Classify this cell by malaria status.
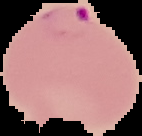

Parasitized.

image type = cell region segmented out of the field of view; surrounding area masked to black
image size = 142×136 pixels
preparation = thin blood film